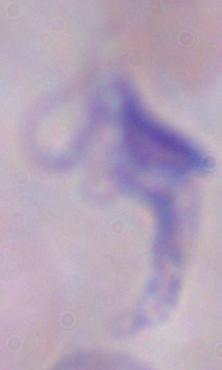
Summary:
  - Identification: trypanosome
  - Magnification: 1000x
  - Modality: photomicrograph